Locate every Plasmodium parasite.
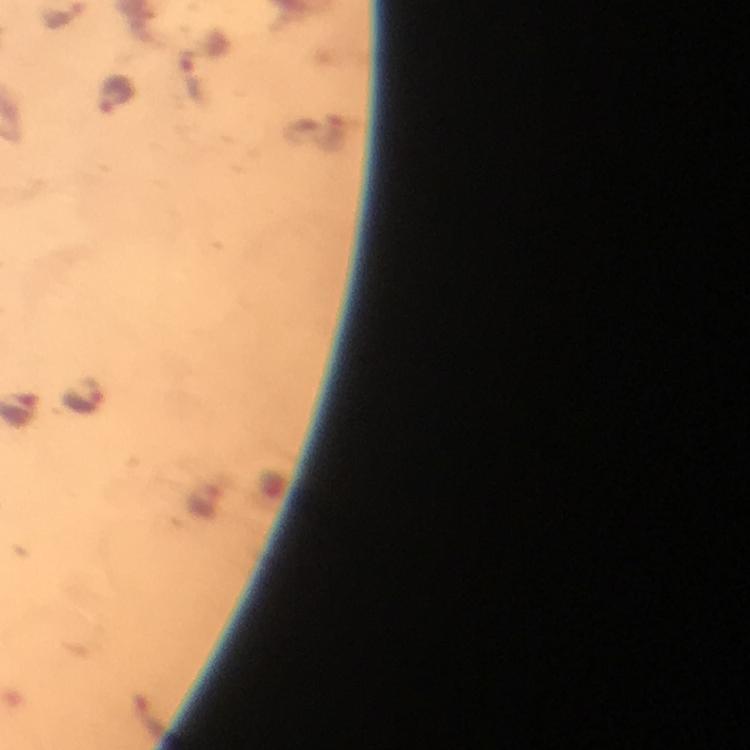
Approximate centers as [x, y] in pixels.
Plasmodium parasites: [196, 79], [115, 94], [80, 398].

At 100x magnification. From a malaria diagnostic workup. Thick blood film. Cropped region of a single field of view. Image is 750×750 pixels. Photographed through the microscope with a smartphone camera. Immersion oil was used. Giemsa stain.